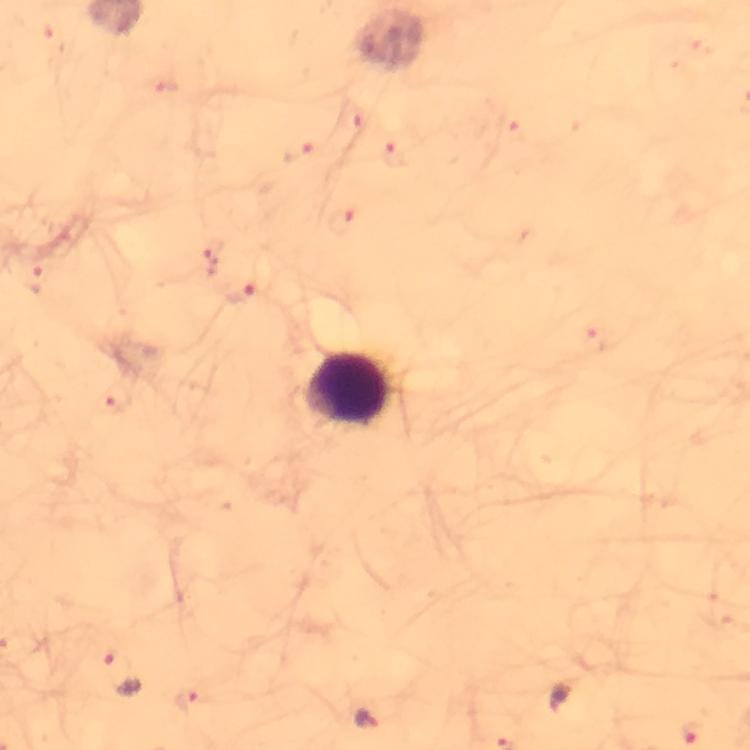
magnification = 100x
image size = 750×750 pixels
context = from a diagnostic examination for malaria
stain = Giemsa
capture = smartphone photograph through a microscope
leukocyte locations = approximate centers as [x, y] in pixels: [347, 388]
Plasmodium parasite locations = approximate centers as [x, y] in pixels: [298, 153], [396, 155], [345, 222], [210, 256], [39, 281], [241, 296], [118, 399], [123, 674], [185, 697], [561, 698], [367, 719]
cropped from = a single field of view
immersion oil = used
preparation = thick blood film